Give the position of every Plasmodium parasite.
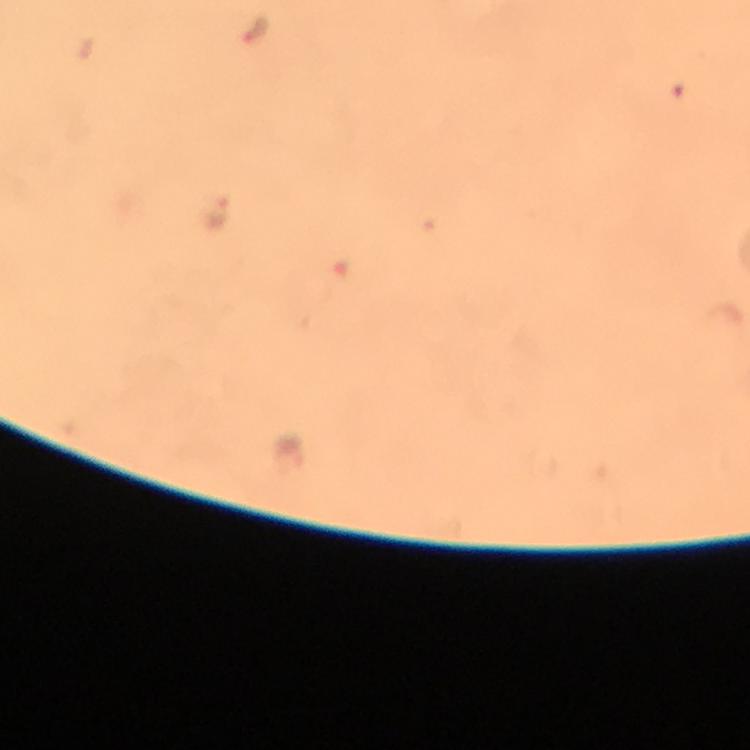

Approximate centers as [x, y] in pixels.
Plasmodium parasites: [215, 215], [290, 453].

Photographed with a smartphone mounted on the microscope. Giemsa stain. A crop from one field of view. Image is 750×750 pixels. At 100x magnification. Thick smear. Immersion oil was used. From a diagnostic examination for malaria.